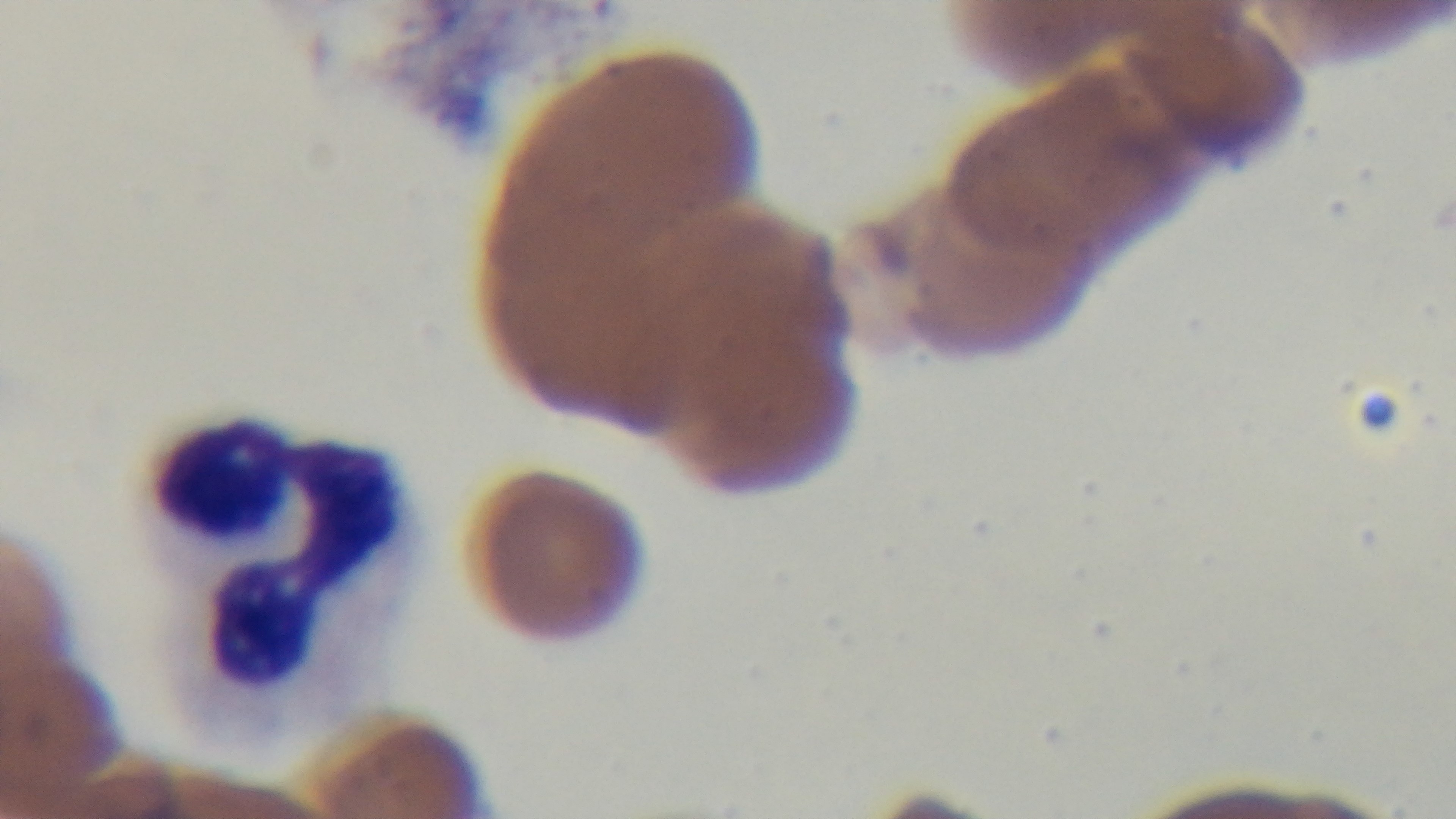

{
  "modality": "light microscopy",
  "field_of_view": "single",
  "objective": "100x oil immersion",
  "malaria_status": "positive",
  "stain": "Giemsa",
  "capture": "mounted 4K digital camera",
  "preparation": "thin smear"
}